Give the extent of all uninfected red blood cells.
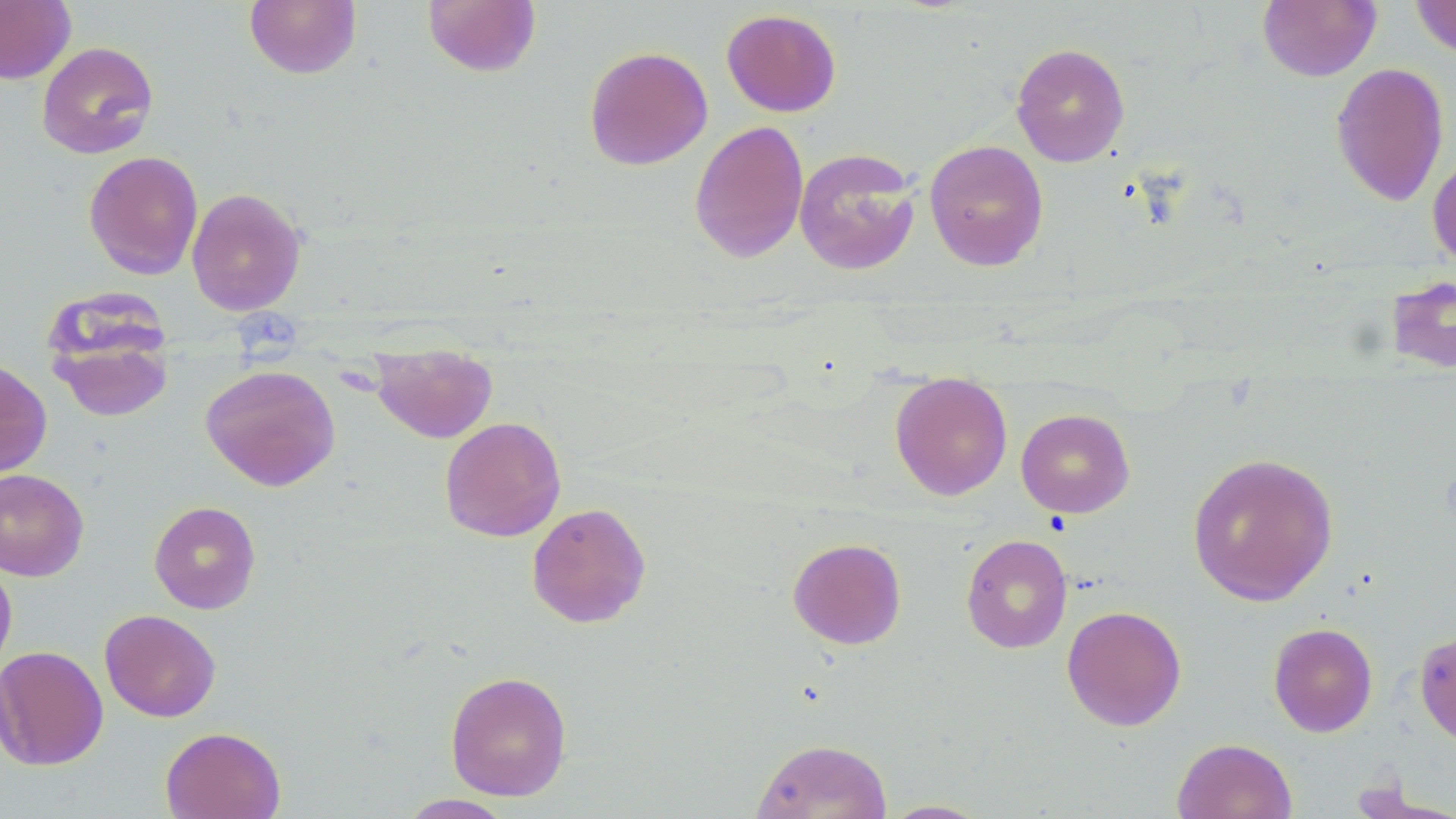
Approximate bounding boxes as (x1, y1, x2, y2) in pixels.
Uninfected red blood cells: (0, 0, 76, 84), (244, 0, 362, 79), (423, 0, 541, 77), (1410, 0, 1456, 59), (1257, 1, 1381, 82), (721, 8, 841, 117), (36, 41, 159, 159), (1010, 42, 1130, 166), (584, 46, 713, 171), (1330, 62, 1449, 207), (689, 120, 809, 264), (924, 139, 1049, 271), (794, 148, 921, 276), (1427, 150, 1456, 271), (83, 151, 203, 279), (186, 187, 306, 316), (1385, 273, 1456, 375), (46, 302, 176, 424), (370, 345, 497, 443), (0, 357, 52, 477), (201, 364, 341, 491), (890, 374, 1013, 500), (1016, 408, 1135, 518), (439, 417, 566, 542), (1186, 452, 1340, 606), (0, 468, 89, 581), (148, 500, 262, 614), (526, 502, 652, 628), (960, 534, 1073, 654), (787, 537, 907, 650), (0, 558, 17, 676), (1061, 605, 1186, 731), (99, 609, 221, 723), (1268, 622, 1378, 737), (1414, 630, 1456, 748), (0, 645, 109, 771), (444, 670, 573, 801), (160, 726, 286, 819), (751, 738, 892, 819), (1172, 738, 1298, 819), (1348, 779, 1454, 819), (396, 793, 517, 818), (879, 799, 993, 818).

Summary:
  - Platelet locations: (232, 309, 302, 368)
  - Slide-level diagnosis: negative for blood parasites
  - Preparation: thin blood smear
  - Modality: light microscopy
  - Magnification: 1000x
  - Image size: 1456×819 pixels
  - Field of view: one of a larger specimen
  - Stain: May-Grünwald-Giemsa